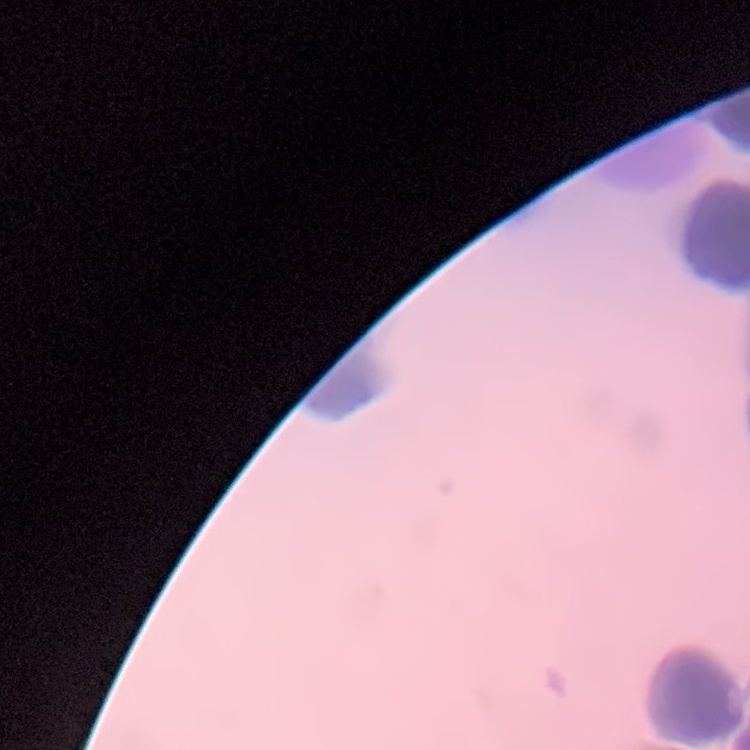

red blood cell morphology = rouleaux formation
image type = one tile cut from a larger photomicrograph
preparation = thin blood film
stain = Field's or Giemsa